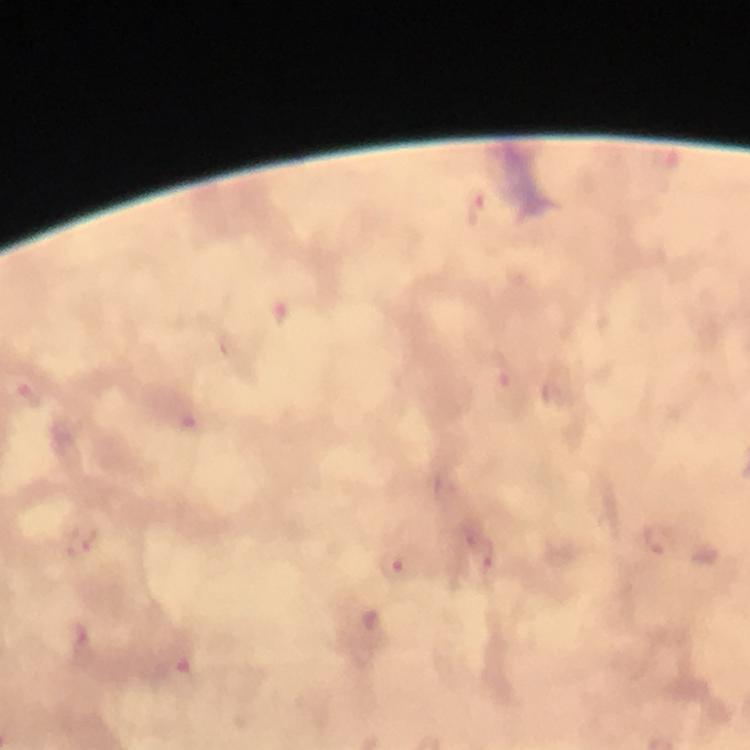

magnification = 100x
context = from a malaria diagnostic workup
immersion oil = applied
stain = Giemsa
Plasmodium parasite locations = approximate centers as (x, y) in pixels: (476, 208), (279, 312), (499, 375), (32, 396), (188, 421), (658, 539), (81, 543), (478, 550), (395, 568), (85, 642), (180, 668)
image size = 750×750 pixels
capture = smartphone photograph through a microscope
cropped from = a single field of view
preparation = thick blood smear